Outline each Plasmodium falciparum-infected red blood cell.
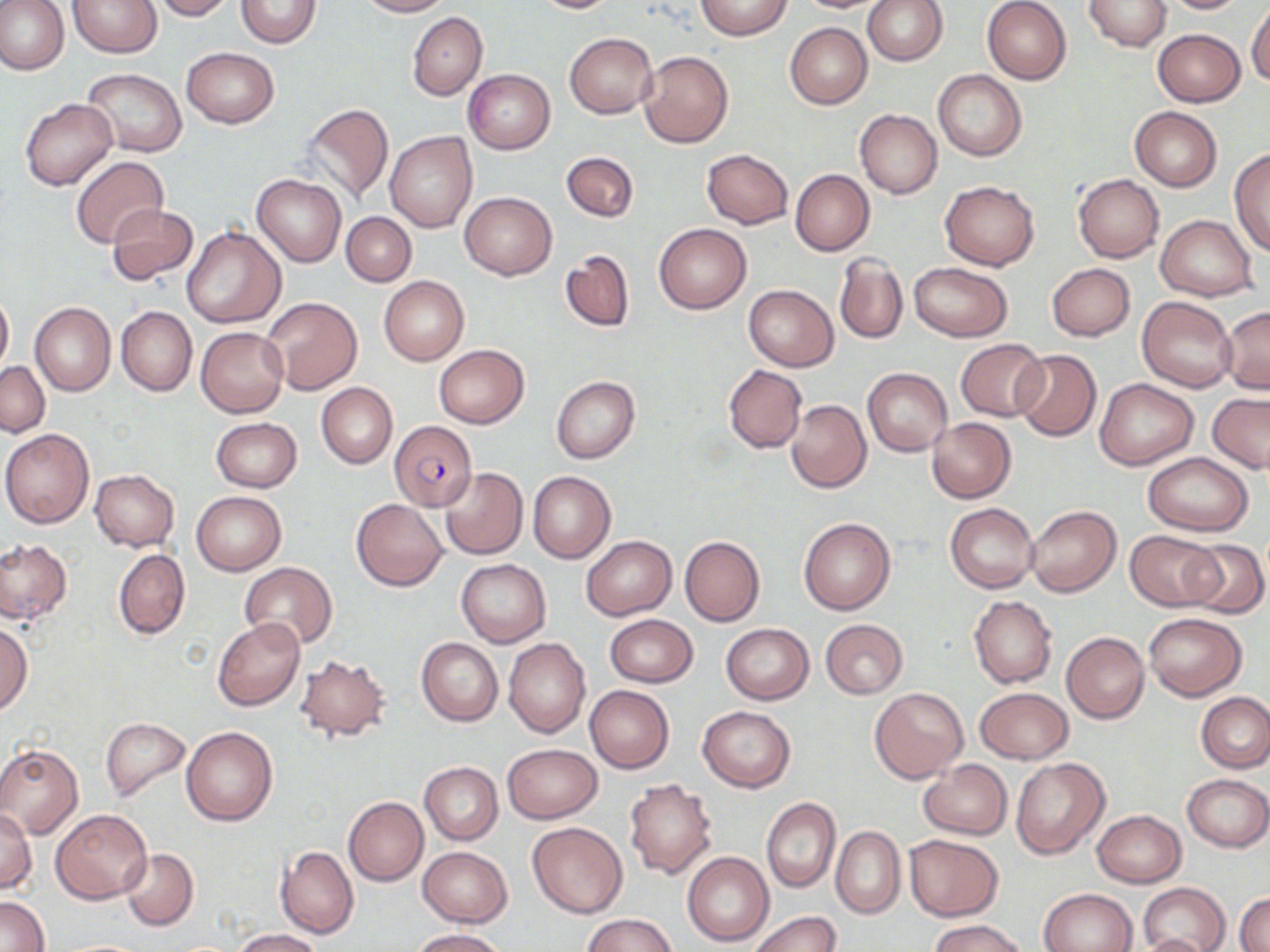
Approximate bounding boxes as named x1/y1/x2/y2 corners in pixels.
Plasmodium falciparum-infected red blood cells: (x1=389, y1=420, x2=478, y2=511).

Summary:
  - Uninfected red blood cell locations: (x1=0, y1=0, x2=68, y2=75), (x1=69, y1=0, x2=161, y2=57), (x1=152, y1=0, x2=234, y2=20), (x1=235, y1=0, x2=321, y2=48), (x1=356, y1=0, x2=450, y2=17), (x1=529, y1=0, x2=622, y2=14), (x1=694, y1=0, x2=794, y2=40), (x1=795, y1=0, x2=893, y2=13), (x1=862, y1=0, x2=947, y2=65), (x1=1083, y1=0, x2=1172, y2=51), (x1=1154, y1=0, x2=1253, y2=14), (x1=981, y1=1, x2=1072, y2=84), (x1=1246, y1=2, x2=1270, y2=87), (x1=407, y1=12, x2=487, y2=100), (x1=784, y1=23, x2=871, y2=110), (x1=1153, y1=29, x2=1245, y2=106), (x1=564, y1=33, x2=658, y2=118), (x1=181, y1=47, x2=278, y2=128), (x1=639, y1=50, x2=733, y2=147), (x1=82, y1=69, x2=186, y2=157), (x1=463, y1=69, x2=555, y2=154), (x1=932, y1=70, x2=1027, y2=160), (x1=19, y1=98, x2=118, y2=190), (x1=299, y1=103, x2=394, y2=204), (x1=1130, y1=107, x2=1222, y2=191), (x1=854, y1=109, x2=942, y2=198), (x1=386, y1=132, x2=477, y2=233), (x1=1230, y1=147, x2=1270, y2=257), (x1=702, y1=149, x2=793, y2=229), (x1=560, y1=151, x2=639, y2=222), (x1=71, y1=155, x2=169, y2=249), (x1=790, y1=169, x2=874, y2=255), (x1=1072, y1=174, x2=1164, y2=262), (x1=252, y1=175, x2=346, y2=266), (x1=938, y1=180, x2=1040, y2=271), (x1=460, y1=191, x2=556, y2=279), (x1=106, y1=205, x2=199, y2=285), (x1=340, y1=212, x2=416, y2=286), (x1=1156, y1=214, x2=1258, y2=301), (x1=654, y1=224, x2=750, y2=314), (x1=180, y1=228, x2=285, y2=329), (x1=560, y1=249, x2=635, y2=333), (x1=834, y1=253, x2=907, y2=346), (x1=907, y1=263, x2=1012, y2=341), (x1=1047, y1=263, x2=1135, y2=341), (x1=378, y1=276, x2=469, y2=366), (x1=743, y1=284, x2=839, y2=371), (x1=0, y1=288, x2=13, y2=378), (x1=260, y1=296, x2=363, y2=395), (x1=1137, y1=297, x2=1237, y2=392), (x1=30, y1=302, x2=115, y2=397), (x1=1220, y1=305, x2=1270, y2=394), (x1=116, y1=306, x2=196, y2=397), (x1=196, y1=327, x2=288, y2=418), (x1=956, y1=339, x2=1048, y2=420), (x1=433, y1=343, x2=529, y2=429), (x1=1013, y1=350, x2=1101, y2=441), (x1=0, y1=361, x2=49, y2=437), (x1=723, y1=366, x2=807, y2=453), (x1=863, y1=368, x2=952, y2=456), (x1=551, y1=375, x2=641, y2=463), (x1=1095, y1=378, x2=1199, y2=470), (x1=316, y1=382, x2=398, y2=468), (x1=1207, y1=393, x2=1269, y2=472), (x1=786, y1=399, x2=871, y2=493), (x1=926, y1=417, x2=1015, y2=502), (x1=212, y1=418, x2=302, y2=492), (x1=1, y1=429, x2=94, y2=528), (x1=1143, y1=453, x2=1254, y2=536), (x1=439, y1=466, x2=527, y2=560), (x1=90, y1=470, x2=179, y2=551), (x1=527, y1=471, x2=616, y2=564), (x1=192, y1=491, x2=287, y2=575), (x1=352, y1=498, x2=448, y2=590), (x1=944, y1=502, x2=1040, y2=594), (x1=1026, y1=505, x2=1121, y2=598), (x1=798, y1=517, x2=896, y2=616), (x1=1124, y1=530, x2=1223, y2=610), (x1=581, y1=535, x2=677, y2=620), (x1=679, y1=536, x2=765, y2=627), (x1=0, y1=537, x2=71, y2=624), (x1=1180, y1=539, x2=1268, y2=618), (x1=113, y1=549, x2=190, y2=640), (x1=456, y1=559, x2=551, y2=647), (x1=240, y1=562, x2=339, y2=651), (x1=968, y1=596, x2=1056, y2=688), (x1=1143, y1=613, x2=1248, y2=701), (x1=605, y1=614, x2=698, y2=688), (x1=212, y1=619, x2=305, y2=710), (x1=820, y1=620, x2=907, y2=698), (x1=0, y1=623, x2=32, y2=714), (x1=721, y1=623, x2=814, y2=704), (x1=1061, y1=632, x2=1149, y2=723), (x1=417, y1=637, x2=503, y2=726), (x1=504, y1=638, x2=590, y2=738), (x1=294, y1=656, x2=392, y2=741), (x1=584, y1=685, x2=674, y2=773), (x1=869, y1=686, x2=969, y2=784), (x1=975, y1=687, x2=1072, y2=763), (x1=1196, y1=693, x2=1269, y2=772), (x1=697, y1=706, x2=796, y2=792), (x1=100, y1=717, x2=191, y2=802), (x1=180, y1=726, x2=277, y2=826), (x1=501, y1=743, x2=602, y2=823), (x1=0, y1=744, x2=84, y2=837), (x1=1010, y1=757, x2=1108, y2=859), (x1=918, y1=759, x2=1011, y2=840), (x1=419, y1=762, x2=503, y2=844), (x1=1182, y1=773, x2=1269, y2=852), (x1=624, y1=779, x2=718, y2=879), (x1=344, y1=796, x2=428, y2=885), (x1=762, y1=798, x2=839, y2=892), (x1=1, y1=808, x2=36, y2=893), (x1=52, y1=809, x2=153, y2=903), (x1=1092, y1=810, x2=1187, y2=887), (x1=527, y1=822, x2=628, y2=918), (x1=830, y1=825, x2=905, y2=919), (x1=904, y1=835, x2=1003, y2=921), (x1=276, y1=844, x2=358, y2=939), (x1=417, y1=846, x2=511, y2=927), (x1=120, y1=847, x2=197, y2=930), (x1=683, y1=851, x2=773, y2=947), (x1=1138, y1=882, x2=1230, y2=952), (x1=1038, y1=888, x2=1138, y2=952), (x1=1236, y1=891, x2=1270, y2=951), (x1=1, y1=895, x2=49, y2=952), (x1=750, y1=911, x2=840, y2=952), (x1=582, y1=913, x2=679, y2=952), (x1=929, y1=918, x2=1028, y2=952), (x1=408, y1=928, x2=505, y2=951), (x1=230, y1=929, x2=324, y2=952), (x1=1136, y1=932, x2=1216, y2=952)
  - Slide-level diagnosis: Plasmodium falciparum
  - Modality: optical microscopy
  - Magnification: 1000x
  - Stain: May-Grünwald-Giemsa
  - Field of view: single
  - Preparation: thin blood smear
  - Image size: 1270×952 pixels